Assess this cell for malaria.
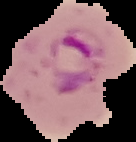

It is parasitized.

image type = cell region segmented out of the field of view; surrounding area masked to black
image size = 136×142 pixels
preparation = thin blood smear